Classify this cell by malaria status.
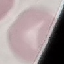

It is uninfected.

Giemsa-stained preparation. Acquired by smartphone through the microscope eyepiece. Automatically extracted cell patch, resized to 64 × 64 pixels. Thin blood smear.